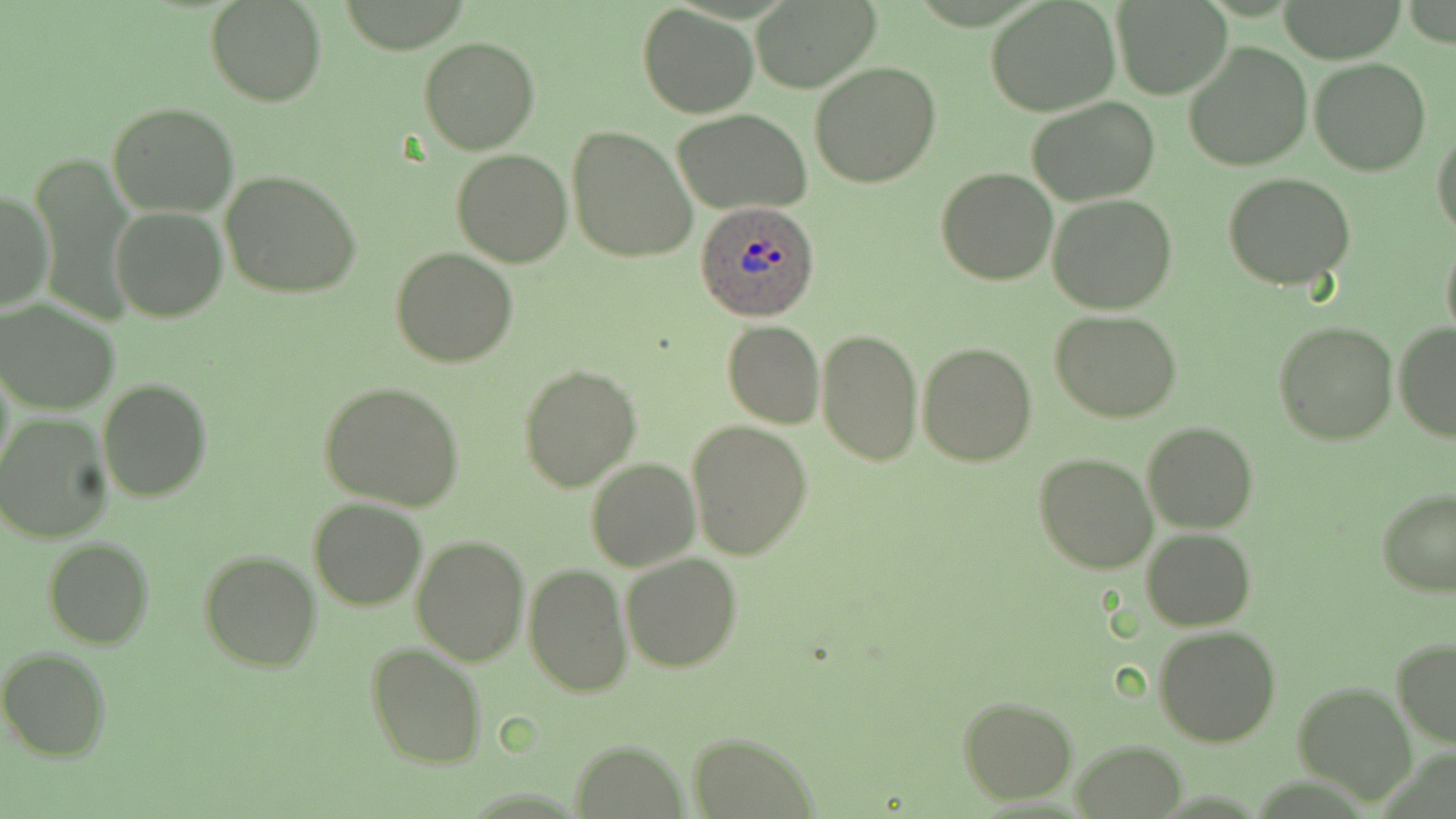

Approximate bounding boxes as (x1,y1)-(x2,y2) corner pairs in pixels. Uninfected red blood cell locations: (986,0)-(1120,116), (205,1)-(327,108), (751,1)-(880,92), (1274,1)-(1409,62), (1113,2)-(1234,100), (638,3)-(758,117), (418,35)-(540,155), (1182,41)-(1313,172), (1309,58)-(1431,176), (810,61)-(942,189), (1026,96)-(1158,205), (107,102)-(240,218), (674,109)-(811,215), (568,124)-(698,266), (1432,126)-(1456,242), (451,148)-(572,267), (31,153)-(135,328), (935,167)-(1058,285), (220,169)-(365,300), (1225,172)-(1355,291), (1,188)-(52,314), (1048,194)-(1178,313), (110,206)-(228,322), (1440,236)-(1456,343), (391,247)-(519,367), (0,299)-(120,416), (1051,309)-(1182,422), (722,320)-(824,430), (1273,321)-(1397,445), (1393,321)-(1456,441), (815,326)-(923,467), (917,341)-(1037,467), (517,364)-(642,493), (98,379)-(211,502), (318,380)-(464,513), (1,414)-(114,544), (687,418)-(815,560), (1141,422)-(1258,533), (1034,452)-(1158,574), (585,458)-(700,572), (1376,488)-(1456,596), (307,498)-(428,611), (1141,527)-(1255,630), (410,533)-(528,666), (43,537)-(154,651), (198,549)-(320,672), (621,554)-(743,673), (522,564)-(631,699), (1154,625)-(1281,747), (1391,638)-(1456,748), (366,642)-(487,770), (0,647)-(111,762), (1294,682)-(1419,806), (958,696)-(1079,804), (688,731)-(818,818), (571,739)-(687,818), (1070,739)-(1186,818). Plasmodium ovale-infected red blood cell locations: (695,200)-(822,322). Slide-level diagnosis: Plasmodium ovale. Thin blood film. Image is 1456×819 pixels. May-Grünwald-Giemsa stain. Light microscopy. 1000x magnification. One field of a larger specimen.